Name the parasite shown.
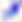
Toxoplasma gondii.

Micrograph. 400x magnification.